Identify the parasite.
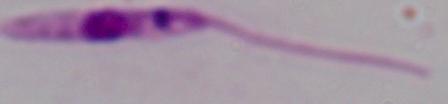
This is Leishmania.

1000x magnification. Micrograph.